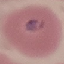

Result: malaria parasites detected. Giemsa-stained preparation. Thin blood film. Photographed with a smartphone camera at the microscope eyepiece. Cell patch, automatically extracted from a larger field of view and resized to 64 × 64 pixels.